State which cell type is depicted.
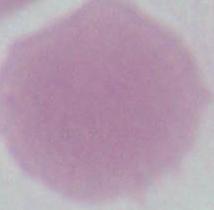

This is an erythrocyte.

Summary:
  - Magnification: 1000x
  - Modality: micrograph